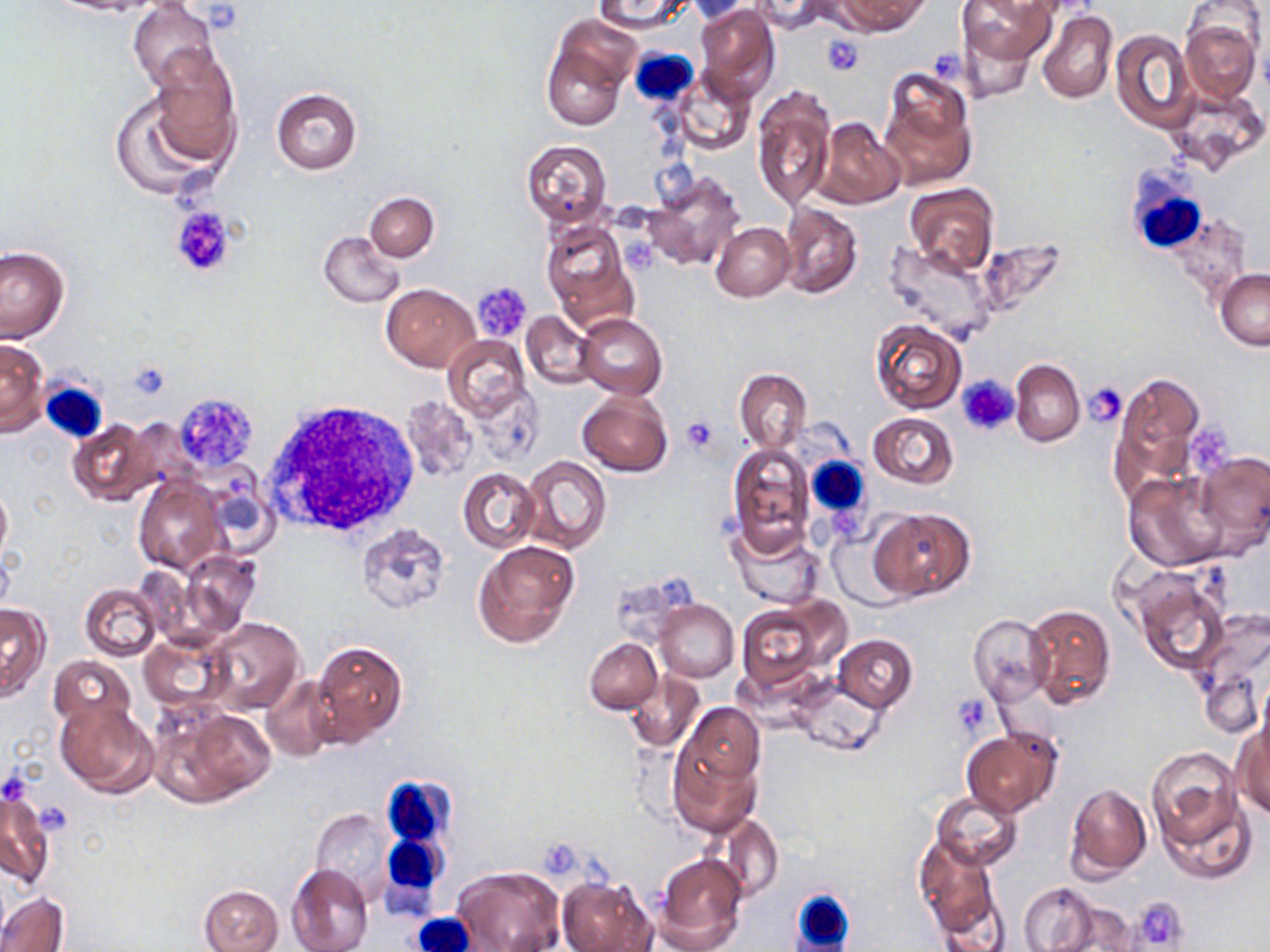
Summary:
  - Coordinate format: approximate bounding boxes as named x1/y1/x2/y2 corners in pixels
  - Platelet locations: (x1=821, y1=34, x2=864, y2=76), (x1=172, y1=208, x2=233, y2=277), (x1=472, y1=283, x2=532, y2=342), (x1=127, y1=362, x2=168, y2=399), (x1=958, y1=376, x2=1019, y2=435), (x1=1084, y1=383, x2=1128, y2=428), (x1=174, y1=390, x2=257, y2=473), (x1=681, y1=416, x2=718, y2=454), (x1=1191, y1=417, x2=1237, y2=470), (x1=953, y1=694, x2=993, y2=737), (x1=1, y1=774, x2=27, y2=807), (x1=37, y1=800, x2=66, y2=843), (x1=538, y1=840, x2=587, y2=878), (x1=1131, y1=896, x2=1191, y2=950)
  - Uninfected red blood cell locations: (x1=44, y1=0, x2=163, y2=17), (x1=591, y1=0, x2=693, y2=32), (x1=751, y1=0, x2=832, y2=34), (x1=837, y1=0, x2=930, y2=35), (x1=960, y1=0, x2=1056, y2=65), (x1=1183, y1=0, x2=1267, y2=69), (x1=684, y1=1, x2=761, y2=24), (x1=128, y1=2, x2=217, y2=90), (x1=693, y1=2, x2=780, y2=100), (x1=1036, y1=9, x2=1117, y2=104), (x1=1179, y1=18, x2=1260, y2=104), (x1=954, y1=21, x2=1044, y2=104), (x1=543, y1=28, x2=632, y2=130), (x1=1113, y1=30, x2=1194, y2=132), (x1=148, y1=48, x2=242, y2=159), (x1=879, y1=68, x2=976, y2=190), (x1=671, y1=70, x2=755, y2=155), (x1=752, y1=85, x2=836, y2=212), (x1=1163, y1=85, x2=1267, y2=174), (x1=108, y1=87, x2=225, y2=201), (x1=270, y1=88, x2=362, y2=174), (x1=814, y1=118, x2=904, y2=208), (x1=521, y1=139, x2=612, y2=227), (x1=641, y1=170, x2=747, y2=272), (x1=904, y1=183, x2=998, y2=278), (x1=364, y1=192, x2=438, y2=261), (x1=778, y1=202, x2=863, y2=298), (x1=541, y1=221, x2=638, y2=330), (x1=710, y1=222, x2=795, y2=301), (x1=318, y1=230, x2=405, y2=309), (x1=884, y1=241, x2=997, y2=345), (x1=0, y1=246, x2=68, y2=342), (x1=1216, y1=268, x2=1270, y2=352), (x1=383, y1=283, x2=479, y2=373), (x1=521, y1=311, x2=597, y2=389), (x1=577, y1=313, x2=667, y2=400), (x1=871, y1=320, x2=966, y2=413), (x1=443, y1=336, x2=530, y2=422), (x1=0, y1=338, x2=47, y2=437), (x1=1010, y1=360, x2=1085, y2=446), (x1=735, y1=369, x2=812, y2=452), (x1=1107, y1=370, x2=1206, y2=504), (x1=577, y1=388, x2=672, y2=478), (x1=401, y1=395, x2=477, y2=483), (x1=867, y1=412, x2=959, y2=489), (x1=66, y1=419, x2=156, y2=507), (x1=727, y1=442, x2=815, y2=556), (x1=1192, y1=449, x2=1270, y2=555), (x1=521, y1=455, x2=611, y2=554), (x1=457, y1=468, x2=539, y2=554), (x1=1123, y1=470, x2=1229, y2=572), (x1=134, y1=479, x2=225, y2=575), (x1=0, y1=481, x2=12, y2=566), (x1=868, y1=507, x2=974, y2=602), (x1=355, y1=523, x2=451, y2=615), (x1=729, y1=526, x2=826, y2=610), (x1=473, y1=540, x2=581, y2=648), (x1=178, y1=549, x2=260, y2=636), (x1=1129, y1=567, x2=1232, y2=674), (x1=81, y1=584, x2=162, y2=660), (x1=655, y1=600, x2=738, y2=682), (x1=735, y1=600, x2=844, y2=692), (x1=0, y1=603, x2=50, y2=701), (x1=1024, y1=603, x2=1116, y2=710), (x1=968, y1=615, x2=1051, y2=705), (x1=1189, y1=615, x2=1269, y2=733), (x1=204, y1=618, x2=305, y2=716), (x1=138, y1=632, x2=227, y2=711), (x1=834, y1=635, x2=917, y2=712), (x1=585, y1=638, x2=662, y2=714), (x1=311, y1=641, x2=407, y2=745), (x1=48, y1=655, x2=137, y2=735), (x1=624, y1=670, x2=705, y2=753), (x1=261, y1=677, x2=338, y2=760), (x1=791, y1=679, x2=885, y2=756), (x1=53, y1=696, x2=158, y2=796), (x1=159, y1=704, x2=275, y2=807), (x1=667, y1=719, x2=762, y2=836), (x1=1232, y1=721, x2=1270, y2=819), (x1=961, y1=728, x2=1062, y2=818), (x1=1146, y1=747, x2=1243, y2=847), (x1=1064, y1=782, x2=1151, y2=879), (x1=1, y1=784, x2=54, y2=891), (x1=931, y1=791, x2=1022, y2=869), (x1=1158, y1=798, x2=1254, y2=884), (x1=310, y1=808, x2=394, y2=901), (x1=709, y1=813, x2=784, y2=902), (x1=915, y1=835, x2=999, y2=940), (x1=654, y1=852, x2=748, y2=952), (x1=286, y1=863, x2=373, y2=952), (x1=450, y1=865, x2=565, y2=952), (x1=558, y1=877, x2=655, y2=952), (x1=1019, y1=884, x2=1100, y2=951), (x1=200, y1=885, x2=283, y2=952), (x1=1, y1=892, x2=67, y2=952), (x1=1047, y1=898, x2=1138, y2=952)
  - White blood cell locations: (x1=628, y1=47, x2=700, y2=104), (x1=1124, y1=169, x2=1211, y2=256), (x1=39, y1=378, x2=109, y2=443), (x1=262, y1=400, x2=422, y2=541), (x1=804, y1=456, x2=871, y2=521), (x1=380, y1=774, x2=454, y2=852), (x1=376, y1=837, x2=446, y2=915), (x1=793, y1=886, x2=852, y2=951), (x1=412, y1=909, x2=479, y2=952)
  - Slide-level diagnosis: no evidence of blood parasites
  - Modality: optical microscopy
  - Magnification: 1000x
  - Preparation: thin blood smear
  - Image size: 1270×952 pixels
  - Stain: May-Grünwald-Giemsa
  - Field of view: one of a larger specimen